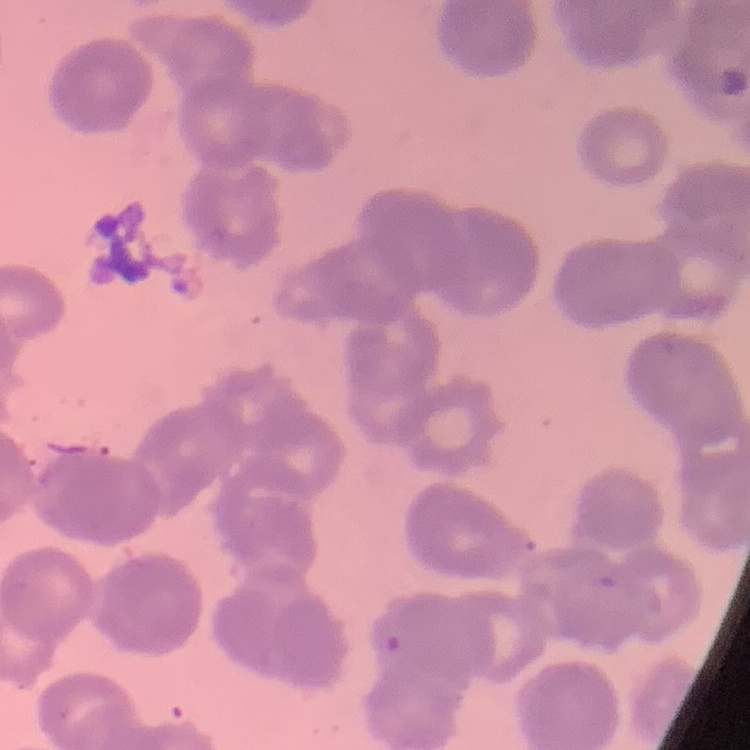

Summary:
  - Erythrocyte morphology: rouleaux formation
  - Stain: Field's or Giemsa
  - Image type: square crop of a larger photomicrograph
  - Preparation: thin blood film